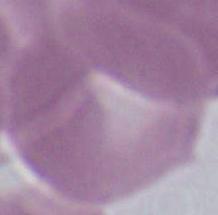

1000x magnification. Micrograph. A red blood cell is seen.